Locate every blood parasite and identify its species.
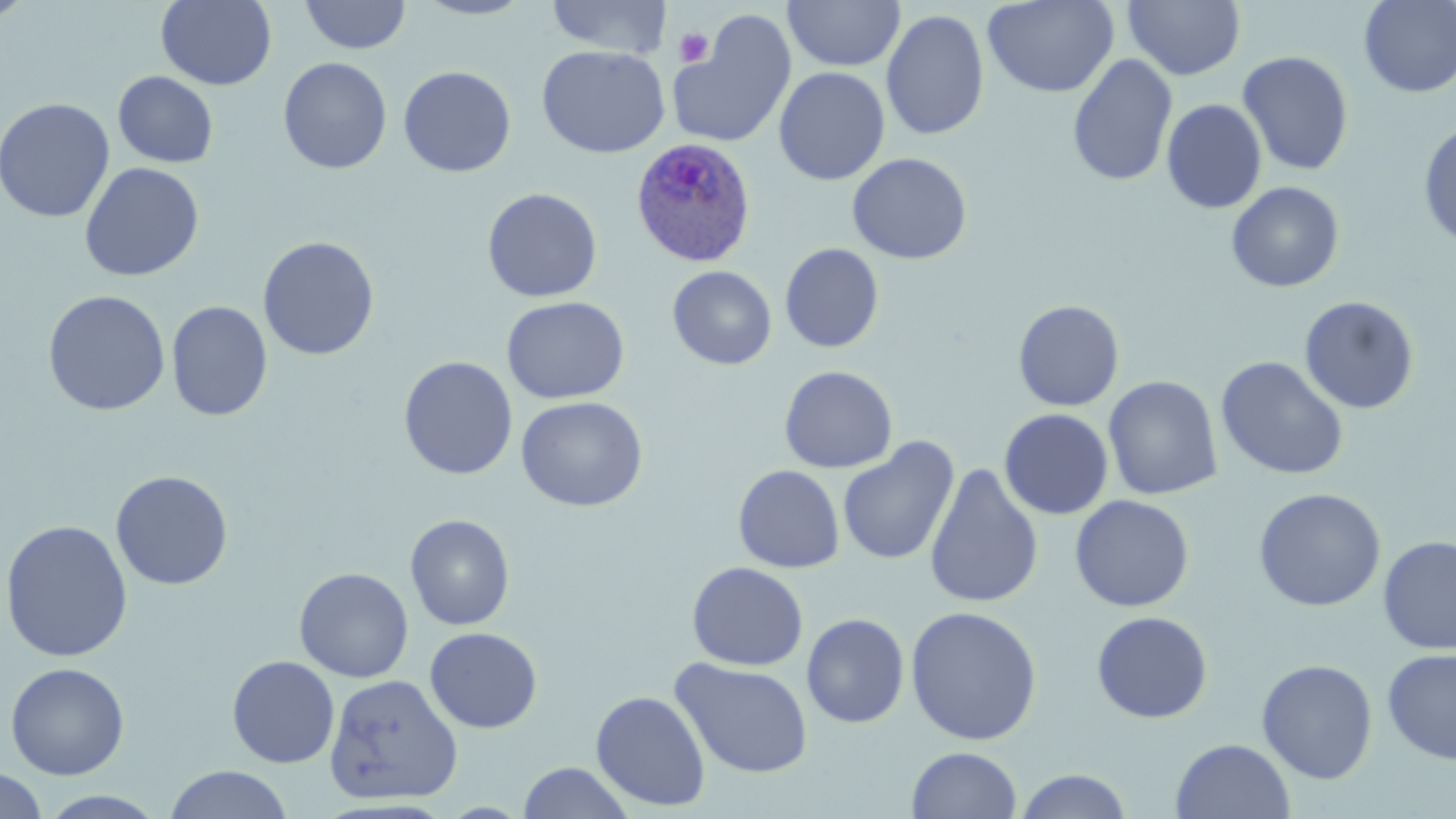

Approximate bounding boxes as (x1, y1, x2, y2) in pixels.
Plasmodium ovale-infected red blood cells: (631, 136, 758, 268).
No Plasmodium falciparum, Plasmodium malariae, Plasmodium vivax, Babesia divergens, or Trypanosoma brucei observed.

slide-level diagnosis = Plasmodium ovale
field of view = single
magnification = 1000x
modality = light microscopy
image size = 1456×819 pixels
preparation = thin blood film
stain = May-Grünwald-Giemsa
uninfected red blood cell locations = approximate bounding boxes as (x1, y1, x2, y2) in pixels: (1, 0, 36, 25), (156, 0, 276, 90), (300, 0, 412, 55), (412, 0, 538, 20), (546, 0, 673, 58), (783, 0, 905, 73), (982, 0, 1119, 98), (1124, 0, 1245, 80), (1358, 1, 1456, 97), (881, 9, 989, 141), (668, 12, 797, 148), (537, 45, 670, 158), (1238, 50, 1354, 176), (1067, 54, 1178, 187), (278, 57, 392, 174), (398, 65, 516, 177), (774, 67, 890, 185), (113, 71, 218, 168), (0, 97, 115, 223), (1162, 99, 1267, 214), (1417, 119, 1456, 251), (847, 153, 972, 264), (79, 162, 204, 282), (1226, 181, 1344, 292), (482, 187, 603, 302), (258, 236, 379, 360), (780, 243, 884, 353), (667, 266, 777, 369), (41, 290, 171, 416), (501, 296, 629, 404), (1299, 296, 1419, 414), (1013, 299, 1124, 411), (166, 300, 272, 421), (398, 355, 518, 480), (1215, 356, 1349, 481), (779, 365, 898, 473), (1103, 376, 1223, 500), (516, 396, 648, 512), (999, 408, 1113, 519), (838, 437, 959, 566), (924, 462, 1044, 610), (733, 464, 844, 573), (110, 470, 233, 590), (1253, 487, 1386, 611), (1070, 494, 1194, 612), (405, 514, 515, 630), (0, 519, 133, 662), (1378, 535, 1456, 654), (686, 561, 809, 671), (294, 567, 414, 682), (905, 605, 1042, 745), (1091, 610, 1213, 723), (802, 613, 910, 728), (424, 627, 543, 733), (1381, 649, 1456, 764), (227, 655, 340, 768), (671, 657, 814, 779), (1256, 659, 1378, 784), (5, 662, 130, 779), (324, 673, 463, 805), (590, 690, 710, 812), (1170, 738, 1296, 819), (907, 747, 1022, 818), (517, 760, 635, 819), (164, 765, 293, 819), (0, 768, 47, 819), (1014, 769, 1133, 818), (39, 790, 168, 818)
platelet locations = approximate bounding boxes as (x1, y1, x2, y2) in pixels: (674, 27, 713, 67)